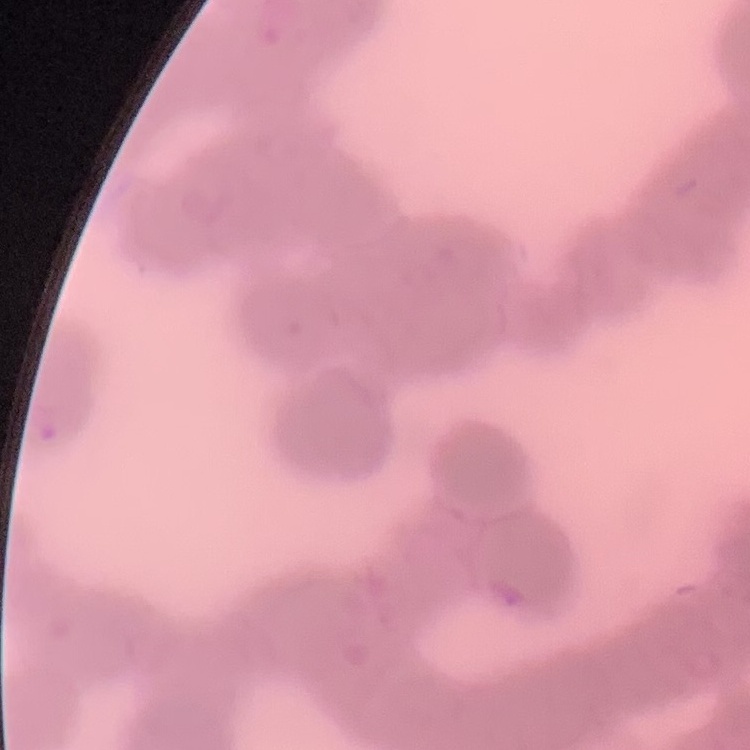
Summary:
  - Erythrocyte morphology: rouleaux formation
  - Image type: square crop of a larger photomicrograph
  - Stain: Field's or Giemsa
  - Preparation: thin blood film